Assess the morphology of the erythrocytes.
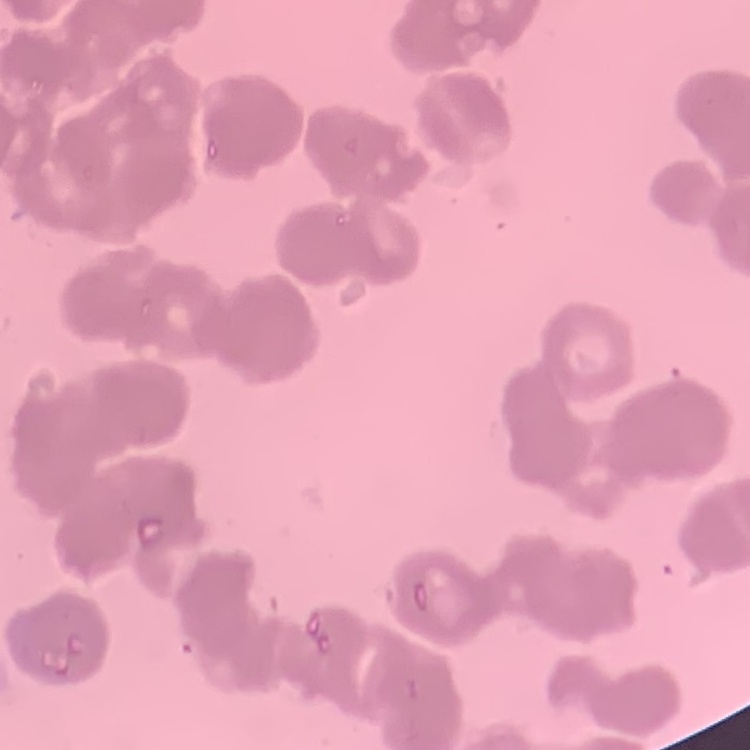

Rouleaux formation.

{
  "stain": "Field's or Giemsa",
  "preparation": "thin blood smear",
  "image_type": "square crop of a larger photomicrograph"
}